Describe the morphology of the red blood cells.
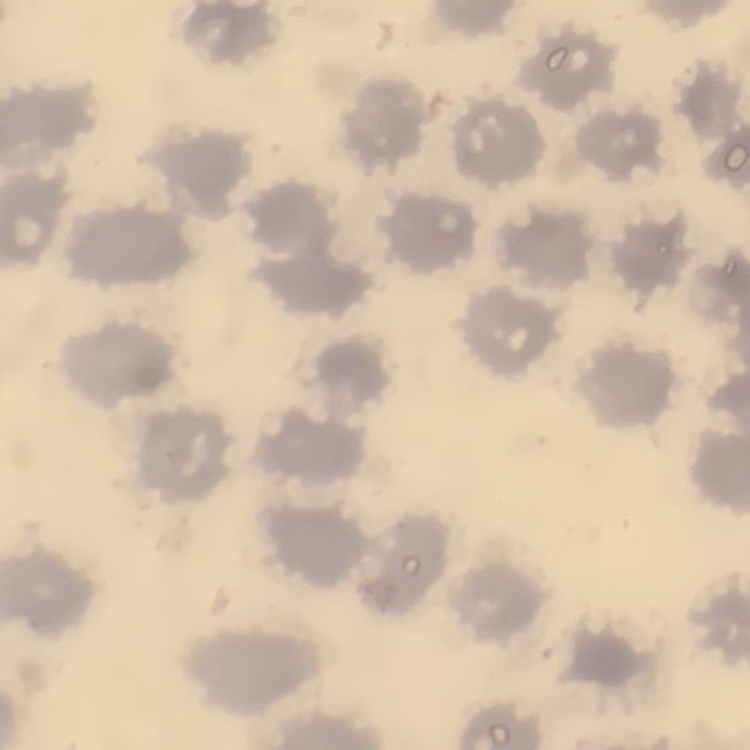

No rouleaux formation.

Summary:
  - Preparation: thin peripheral smear
  - Stain: Field's or Giemsa
  - Image type: square crop of a larger photomicrograph